Find the cells and give the type of each one.
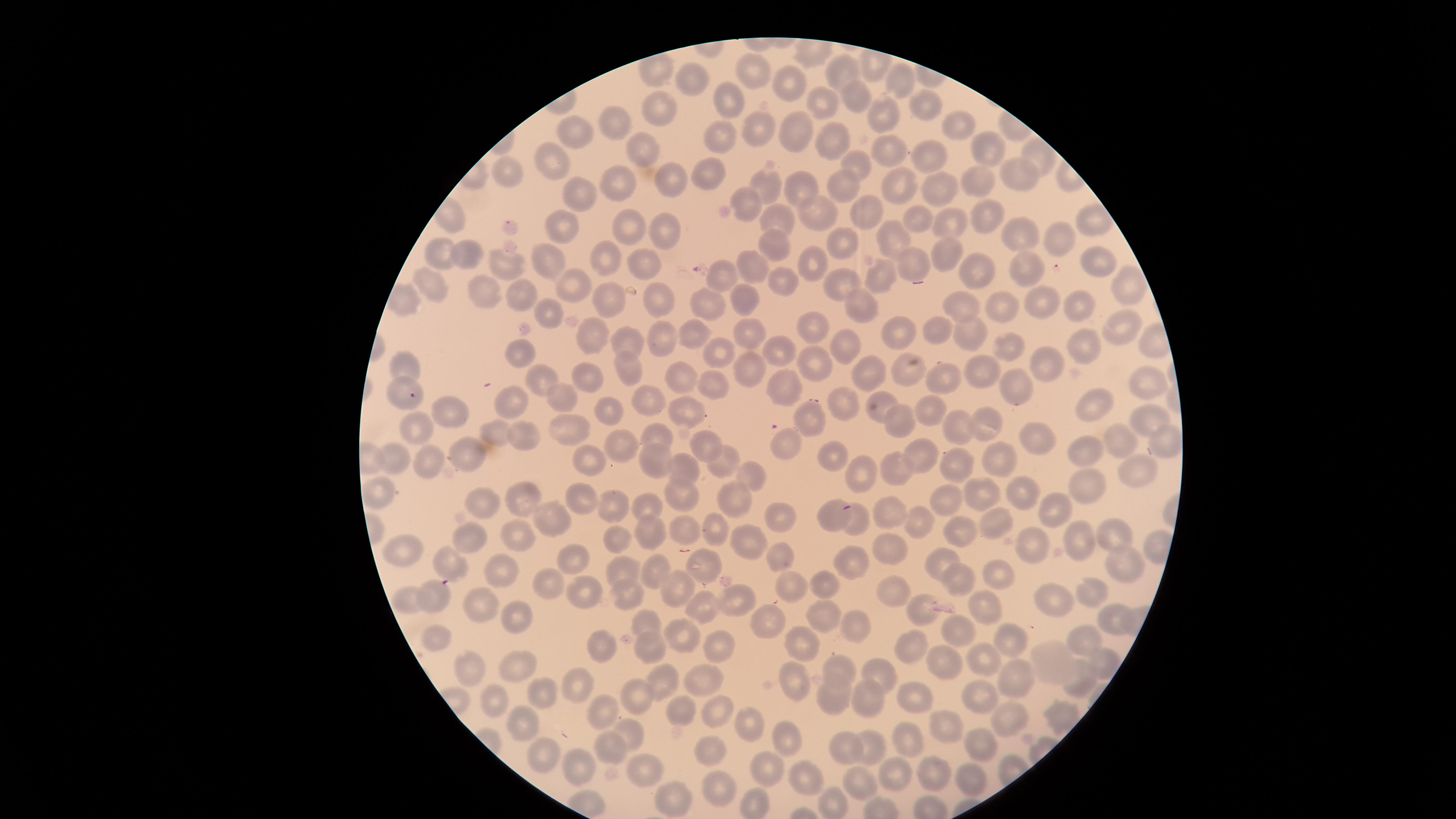
No parasitized red blood cells identified.
Approximate marker points as {x, y} in pixels.
Uninfected red blood cells: {844, 70}, {758, 77}, {792, 80}, {902, 81}, {699, 85}, {860, 95}, {735, 98}, {821, 103}, {924, 105}, {662, 110}, {881, 117}, {619, 120}, {954, 124}, {797, 130}, {756, 131}, {580, 132}, {727, 135}, {835, 138}, {644, 148}, {988, 151}, {886, 152}, {930, 154}, {1041, 155}, {549, 162}, {856, 164}, {1021, 167}, {710, 169}, {510, 171}, {671, 179}, {979, 179}, {765, 181}, {801, 182}, {844, 185}, {902, 185}, {618, 187}, {941, 187}, {577, 193}, {752, 197}, {810, 210}, {859, 210}, {980, 215}, {920, 216}, {558, 223}, {781, 223}, {628, 225}, {664, 227}, {953, 227}, {1014, 236}, {893, 239}, {851, 240}, {1064, 241}, {774, 247}, {947, 251}, {446, 253}, {464, 253}, {603, 260}, {642, 261}, {547, 262}, {1092, 262}, {503, 264}, {814, 264}, {752, 265}, {913, 265}, {1029, 267}, {973, 269}, {726, 277}, {882, 278}, {784, 281}, {843, 285}, {431, 286}, {575, 289}, {1127, 291}, {485, 294}, {517, 296}, {1043, 296}, {657, 297}, {613, 300}, {741, 300}, {711, 303}, {858, 307}, {959, 307}, {1010, 308}, {1078, 309}, {547, 313}, {1120, 325}, {928, 329}, {972, 330}, {814, 331}, {900, 333}, {594, 334}, {694, 335}, {746, 335}, {659, 338}, {633, 342}, {1087, 343}, {848, 344}, {721, 348}, {1008, 348}, {777, 353}, {520, 355}, {811, 360}, {1050, 363}, {403, 365}, {983, 367}, {627, 369}, {749, 369}, {911, 369}, {591, 373}, {865, 373}, {685, 375}, {940, 380}, {540, 384}, {716, 385}, {1014, 387}, {784, 388}, {1148, 389}, {401, 394}, {567, 397}, {649, 398}, {514, 400}, {882, 405}, {1097, 405}, {609, 406}, {841, 407}, {684, 409}, {932, 409}, {452, 413}, {1143, 413}, {418, 425}, {809, 425}, {897, 425}, {984, 426}, {960, 429}, {559, 430}, {494, 434}, {654, 435}, {518, 436}, {1040, 437}, {1120, 439}, {1161, 442}, {704, 444}, {618, 447}, {779, 447}, {472, 455}, {920, 455}, {1087, 455}, {587, 459}, {648, 459}, {995, 459}, {394, 462}, {832, 462}, {434, 463}, {720, 464}, {681, 468}, {892, 469}, {960, 469}, {865, 471}, {1139, 477}, {752, 478}, {1081, 484}, {376, 489}, {583, 495}, {679, 495}, {983, 495}, {1022, 496}, {646, 501}, {731, 501}, {524, 502}, {953, 502}, {482, 506}, {608, 508}, {1058, 508}, {828, 514}, {886, 514}, {775, 515}, {549, 516}, {991, 522}, {856, 525}, {707, 526}, {915, 527}, {648, 529}, {682, 529}, {961, 533}, {522, 534}, {1115, 534}, {615, 539}, {748, 539}, {465, 540}, {1073, 541}, {401, 545}, {1032, 545}, {893, 547}, {781, 552}, {570, 556}, {1119, 560}, {847, 562}, {449, 564}, {941, 565}, {703, 567}, {621, 569}, {1001, 572}, {652, 573}, {493, 575}, {551, 582}, {789, 582}, {956, 582}, {824, 585}, {674, 589}, {889, 594}, {1089, 594}, {623, 595}, {589, 596}, {436, 597}, {408, 599}, {737, 600}, {1056, 604}, {483, 605}, {982, 605}, {701, 606}, {921, 611}, {824, 617}, {1110, 618}, {515, 619}, {645, 620}, {851, 623}, {765, 625}, {957, 630}, {676, 632}, {1079, 632}, {1009, 638}, {601, 640}, {435, 641}, {808, 644}, {714, 646}, {649, 647}, {909, 647}, {1101, 658}, {980, 660}, {1051, 663}, {948, 665}, {469, 672}, {514, 672}, {834, 673}, {1076, 675}, {698, 676}, {879, 676}, {1016, 677}, {666, 681}, {796, 684}, {577, 686}, {546, 691}, {910, 693}, {978, 693}, {638, 697}, {831, 699}, {867, 702}, {500, 707}, {604, 710}, {715, 712}, {678, 713}, {1059, 715}, {526, 719}, {1010, 722}, {746, 725}, {947, 728}, {634, 731}, {786, 736}, {976, 742}, {910, 744}, {612, 747}, {843, 748}, {871, 749}, {543, 756}, {707, 757}, {578, 767}, {770, 768}, {933, 772}, {643, 776}, {971, 776}, {895, 778}, {806, 780}, {858, 783}, {716, 791}, {758, 804}, {832, 804}, {668, 805}.
No white blood cells identified.

Image is 1456×819 pixels. The visible region is circular. Giemsa-stained preparation. Photographed with a smartphone camera through the microscope eyepiece. Single field of view. Thin smear of blood.